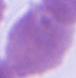
1000x magnification. An erythrocyte is seen. Micrograph.